Identify the blood parasite species.
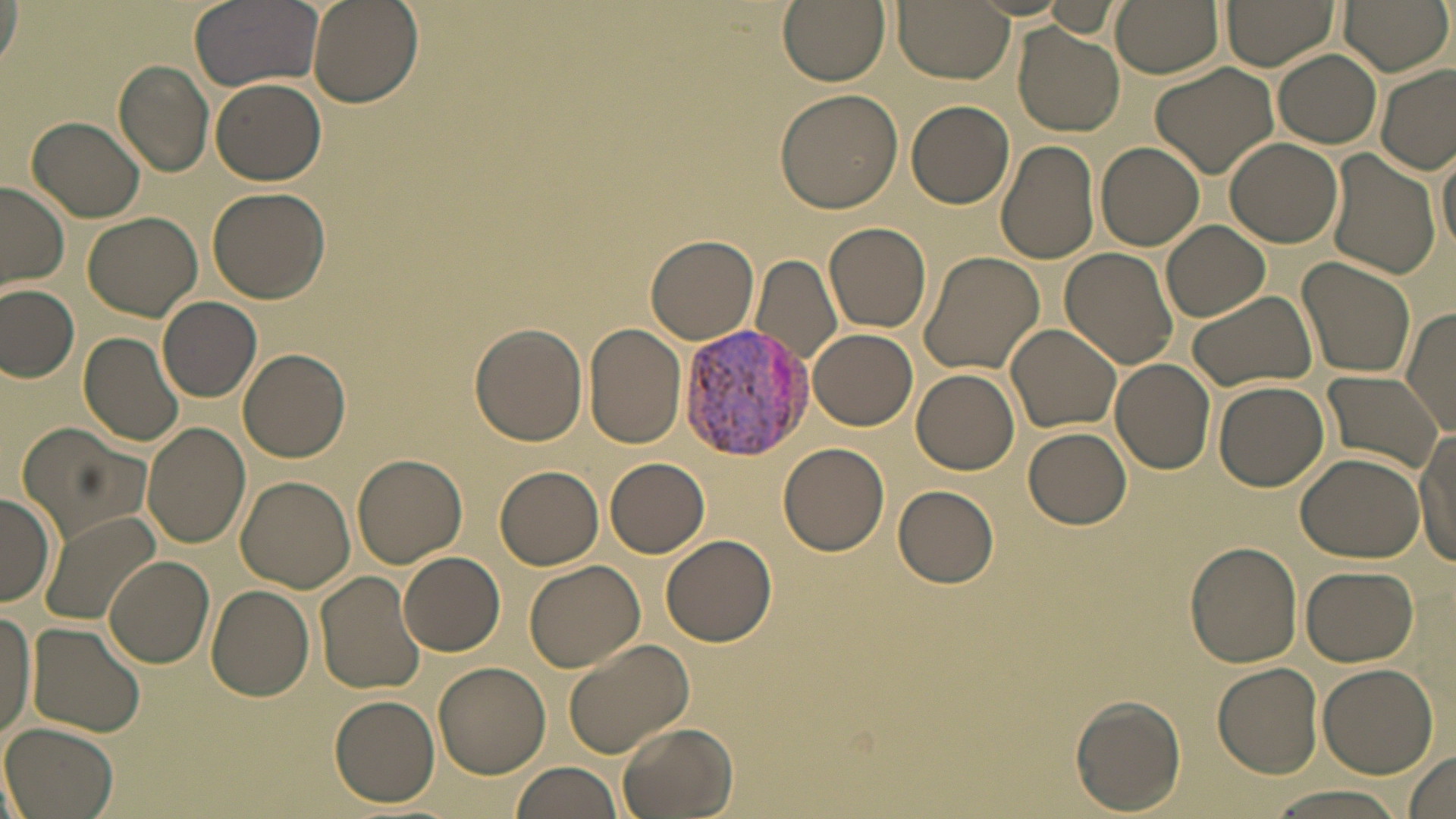

Plasmodium vivax.

Approximate bounding boxes as [x1, y1, x2, y2] in pixels. Uninfected red blood cell locations: [190, 0, 323, 90], [307, 0, 423, 108], [777, 0, 890, 86], [892, 0, 1014, 84], [1111, 0, 1224, 78], [1222, 0, 1340, 71], [1341, 0, 1449, 75], [1038, 1, 1126, 39], [0, 2, 23, 78], [1012, 25, 1124, 135], [1274, 50, 1381, 148], [113, 61, 215, 179], [1150, 62, 1279, 179], [1374, 65, 1455, 175], [210, 76, 326, 185], [774, 89, 902, 214], [906, 101, 1014, 209], [27, 115, 145, 222], [1225, 138, 1344, 249], [995, 140, 1100, 265], [1436, 141, 1456, 258], [1097, 142, 1204, 250], [1324, 150, 1441, 281], [0, 183, 70, 292], [207, 188, 329, 302], [82, 211, 202, 321], [825, 221, 932, 333], [1161, 221, 1269, 321], [647, 234, 759, 344], [1061, 249, 1179, 369], [916, 250, 1044, 375], [752, 253, 841, 368], [1296, 255, 1417, 380], [0, 284, 80, 383], [1185, 289, 1317, 394], [159, 296, 261, 401], [1400, 306, 1456, 436], [469, 321, 589, 445], [583, 322, 686, 449], [1006, 323, 1122, 433], [810, 328, 918, 429], [79, 329, 186, 447], [237, 348, 350, 463], [1110, 357, 1217, 474], [912, 367, 1020, 474], [1320, 369, 1443, 473], [1213, 381, 1329, 492], [17, 422, 149, 543], [143, 422, 250, 549], [1024, 427, 1132, 530], [1414, 432, 1456, 562], [778, 442, 889, 555], [1295, 452, 1425, 563], [352, 453, 466, 568], [605, 458, 710, 558], [494, 466, 603, 570], [235, 476, 355, 591], [894, 486, 1000, 587], [1, 493, 56, 609], [39, 510, 162, 628], [661, 534, 778, 648], [1184, 541, 1303, 668], [398, 550, 504, 656], [106, 556, 214, 668], [523, 559, 646, 674], [1301, 565, 1419, 666], [315, 570, 426, 694], [205, 585, 314, 700], [0, 610, 36, 742], [28, 620, 148, 736], [561, 639, 694, 759], [433, 662, 551, 778], [1213, 662, 1323, 778], [1317, 664, 1439, 778], [330, 694, 440, 806], [1070, 694, 1187, 815], [2, 722, 118, 819], [618, 722, 740, 819], [1401, 750, 1455, 818], [509, 762, 621, 819], [1265, 788, 1409, 819]. Plasmodium vivax-infected red blood cell locations: [677, 322, 815, 459]. Thin blood smear. One field of a larger specimen. May-Grünwald-Giemsa stain. Image is 1456×819 pixels. Optical microscopy. 1000x magnification.